Comment on the morphology of the red blood cells.
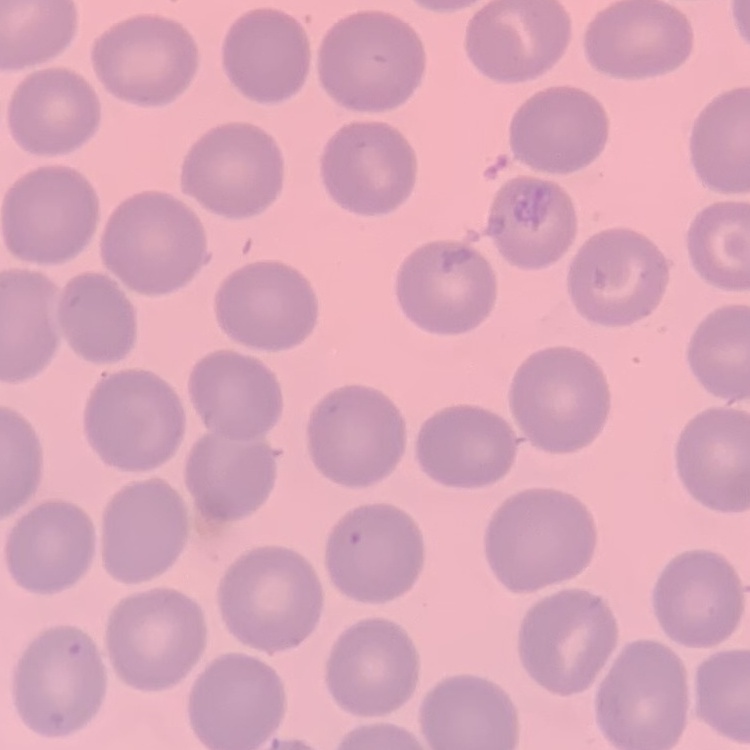

They show no rouleaux formation.

image type = square crop of a larger photomicrograph
stain = Field's or Giemsa
preparation = thin peripheral smear